Give the extent of all Plasmodium ovale-infected red blood cells.
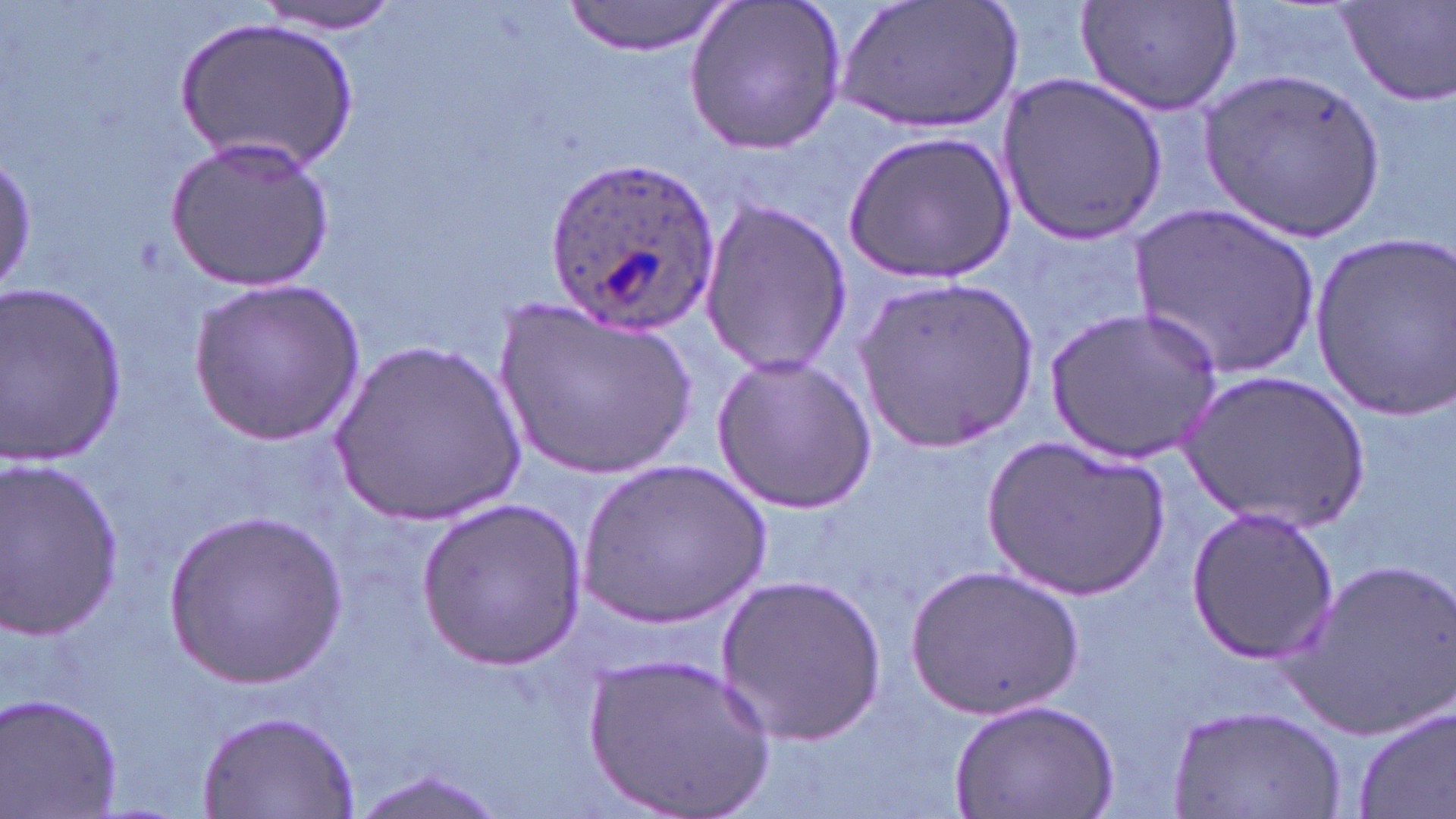

Approximate bounding boxes as [x1, y1, x2, y2] in pixels.
Plasmodium ovale-infected red blood cells: [545, 155, 719, 332].

Summary:
  - Uninfected red blood cell locations: [561, 0, 734, 57], [682, 0, 847, 158], [833, 0, 1030, 138], [1079, 0, 1243, 118], [253, 1, 406, 33], [1334, 1, 1456, 108], [176, 17, 356, 172], [1204, 70, 1386, 239], [997, 71, 1170, 242], [842, 129, 1013, 284], [164, 137, 337, 293], [0, 148, 36, 297], [697, 199, 851, 376], [1132, 202, 1320, 380], [1306, 229, 1455, 421], [859, 275, 1039, 453], [187, 278, 364, 444], [0, 280, 128, 468], [494, 296, 702, 484], [1049, 306, 1222, 461], [330, 339, 526, 525], [710, 354, 876, 515], [1178, 372, 1368, 526], [984, 434, 1170, 598], [0, 457, 125, 637], [577, 458, 774, 632], [414, 498, 591, 668], [1185, 504, 1341, 663], [161, 510, 344, 686], [1285, 556, 1456, 737], [908, 564, 1081, 716], [718, 572, 886, 745], [585, 652, 774, 819], [1, 692, 122, 819], [949, 697, 1121, 817], [1170, 701, 1349, 816], [1354, 705, 1455, 819], [197, 706, 364, 818], [346, 766, 505, 819]
  - Slide-level diagnosis: Plasmodium ovale
  - Stain: May-Grünwald-Giemsa
  - Magnification: 1000x
  - Modality: light microscopy
  - Field of view: one of a larger specimen
  - Preparation: thin blood smear
  - Image size: 1456×819 pixels